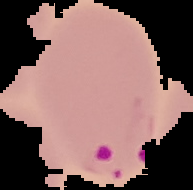
Summary:
  - Image type: segmented cell region on a black background
  - Image size: 193×190 pixels
  - Preparation: thin blood smear
  - Malaria status: parasitized